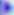
identification: Toxoplasma gondii
magnification: 400x
modality: photomicrograph